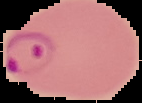
From a thin blood smear. Image is 142×103 pixels. Segmented cell region on a black background. Result: malaria parasites identified.